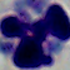

Summary:
  - Identification: leukocyte
  - Modality: photomicrograph
  - Magnification: 1000x